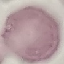
Malaria status: uninfected. Giemsa-stained preparation. Automatically extracted cell patch, resized to 64 × 64 pixels. Thin blood smear. Photographed with a smartphone camera at the microscope eyepiece.